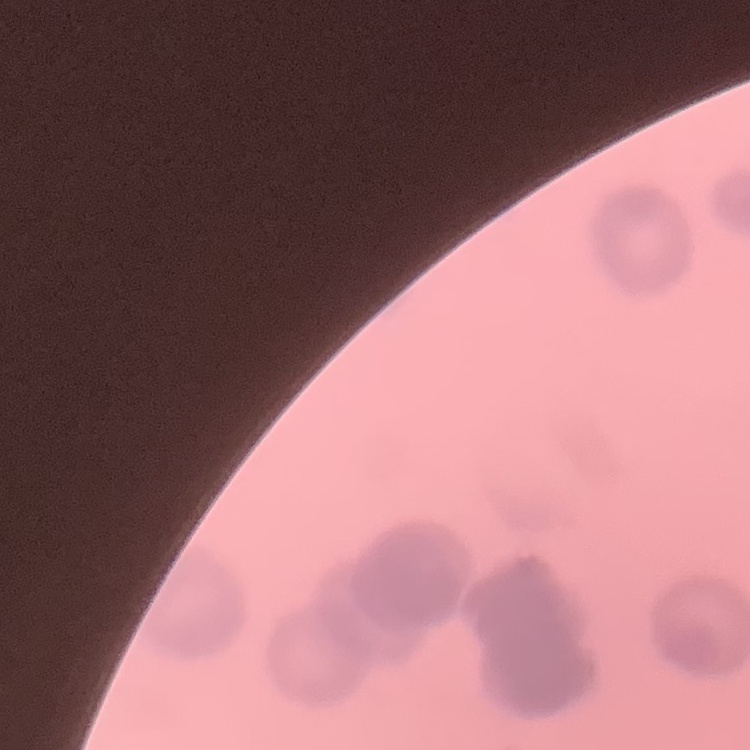

red_blood_cell_morphology: rouleaux formation
preparation: thin peripheral smear
image_type: square crop of a larger photomicrograph
stain: Field's or Giemsa